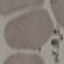 Result: no malaria parasites seen. Thin blood smear. Acquired by smartphone through the microscope eyepiece. Cell patch, automatically extracted from a larger field of view and resized to 64 × 64 pixels. Giemsa stain.